Locate every blood parasite and identify its species.
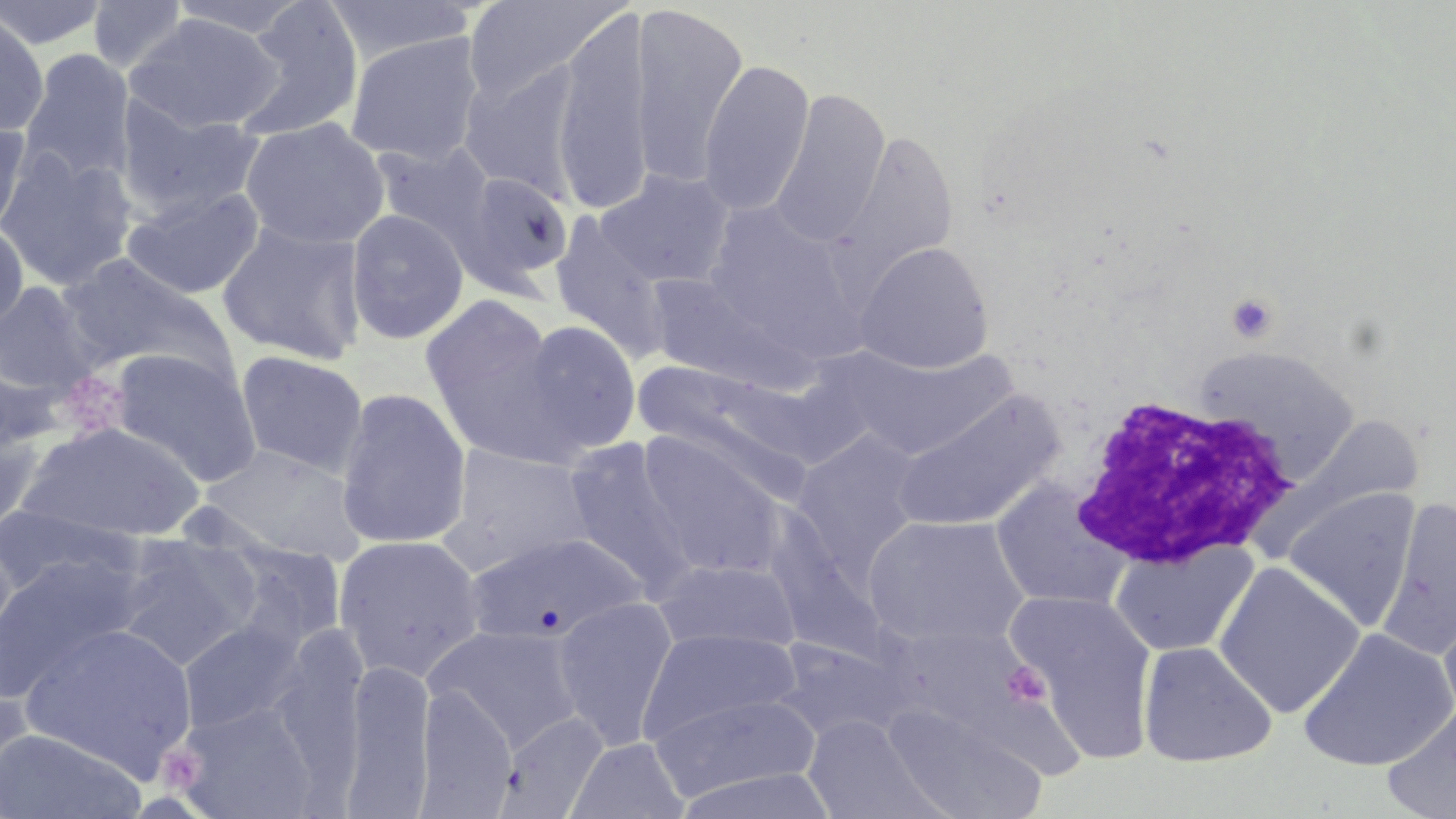
No blood parasites seen.

Summary:
  - Coordinate format: approximate bounding boxes as [x1, y1, x2, y2] in pixels
  - Platelet locations: [1225, 293, 1279, 343], [1002, 661, 1051, 707], [156, 743, 205, 795]
  - Uninfected red blood cell locations: [0, 0, 111, 51], [165, 0, 315, 39], [322, 0, 478, 64], [461, 0, 623, 102], [86, 1, 191, 73], [230, 1, 366, 144], [630, 4, 748, 187], [0, 9, 50, 137], [552, 11, 655, 215], [124, 13, 282, 133], [344, 31, 484, 166], [18, 48, 136, 186], [458, 60, 585, 202], [698, 60, 815, 216], [769, 89, 890, 247], [114, 98, 267, 221], [240, 117, 390, 251], [0, 119, 32, 239], [834, 130, 960, 281], [369, 140, 497, 254], [0, 148, 139, 291], [596, 169, 735, 288], [455, 171, 574, 294], [121, 185, 266, 300], [345, 208, 469, 345], [548, 213, 672, 362], [217, 219, 368, 365], [0, 221, 30, 337], [854, 241, 994, 374], [59, 253, 237, 387], [644, 271, 794, 390], [0, 282, 102, 398], [420, 293, 569, 459], [516, 319, 642, 456], [833, 344, 1019, 461], [1193, 344, 1360, 481], [108, 348, 263, 487], [234, 350, 369, 477], [633, 358, 818, 490], [334, 386, 472, 551], [891, 389, 1064, 532], [1302, 415, 1424, 510], [0, 419, 46, 538], [16, 421, 205, 542], [790, 429, 926, 577], [636, 431, 790, 580], [562, 439, 698, 598], [440, 442, 598, 577], [197, 445, 368, 562], [991, 480, 1132, 612], [1283, 486, 1420, 631], [1379, 498, 1456, 662], [0, 503, 142, 601], [862, 514, 1030, 649], [463, 531, 646, 644], [332, 533, 487, 683], [111, 534, 260, 670], [210, 538, 347, 658], [1111, 540, 1259, 658], [0, 552, 145, 699], [651, 559, 802, 654], [1213, 561, 1365, 719], [1009, 589, 1158, 759], [553, 594, 679, 749], [1439, 608, 1456, 731], [177, 619, 310, 734], [424, 624, 587, 754], [20, 625, 201, 776], [636, 626, 803, 745], [1297, 628, 1456, 772], [769, 636, 916, 744], [1138, 641, 1277, 768], [343, 652, 436, 817], [0, 685, 37, 809], [415, 685, 518, 816], [648, 692, 823, 802], [173, 702, 324, 818], [1381, 702, 1456, 819], [883, 704, 1048, 819], [495, 711, 609, 817], [803, 717, 935, 817], [0, 728, 147, 819], [565, 737, 690, 819]
  - White blood cell locations: [1063, 396, 1297, 574]
  - Slide-level diagnosis: no evidence of blood parasites
  - Preparation: thin blood smear
  - Stain: May-Grünwald-Giemsa
  - Image size: 1456×819 pixels
  - Magnification: 1000x
  - Modality: optical microscopy
  - Field of view: one of a larger specimen